Report the malaria status of this cell.
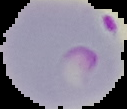
Parasitized.

Summary:
  - Image size: 127×109 pixels
  - Image type: segmented cell region with the area outside set to black
  - Preparation: thin blood smear